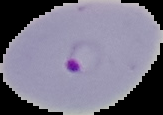

malaria status = parasitized
preparation = thin blood film
image type = segmented cell region with the area outside set to black
image size = 163×115 pixels